Name the parasite shown.
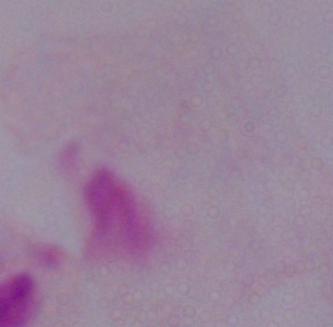

This is a trichomonad.

modality = photomicrograph
magnification = 1000x